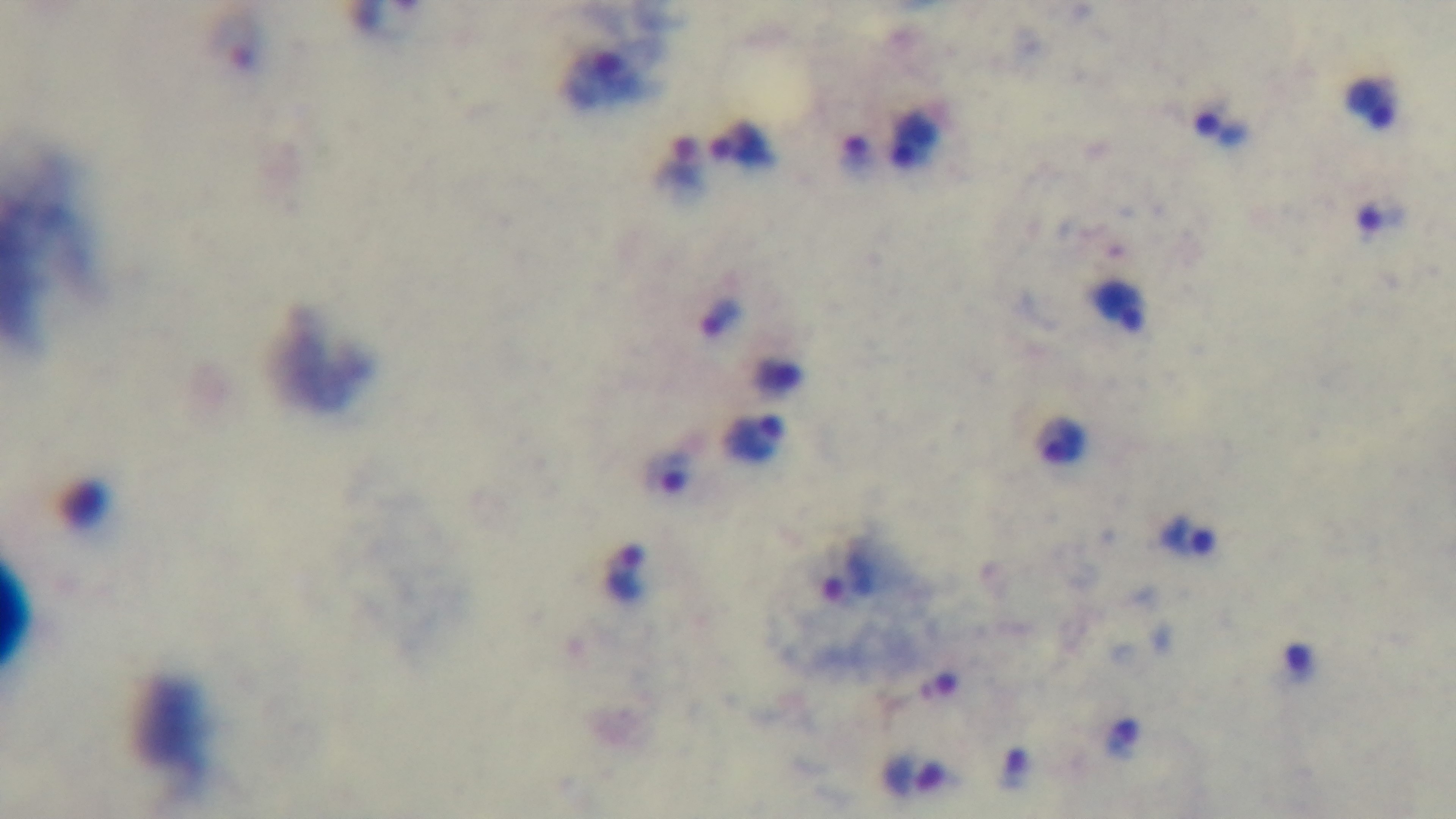

Oil-immersion objective, 100x. Photomicrograph. Preparation: thick blood film. Giemsa stain. Mounted 4K digital camera. Single field of view. Malaria status: infected.